Give the position of every leukocyte visible.
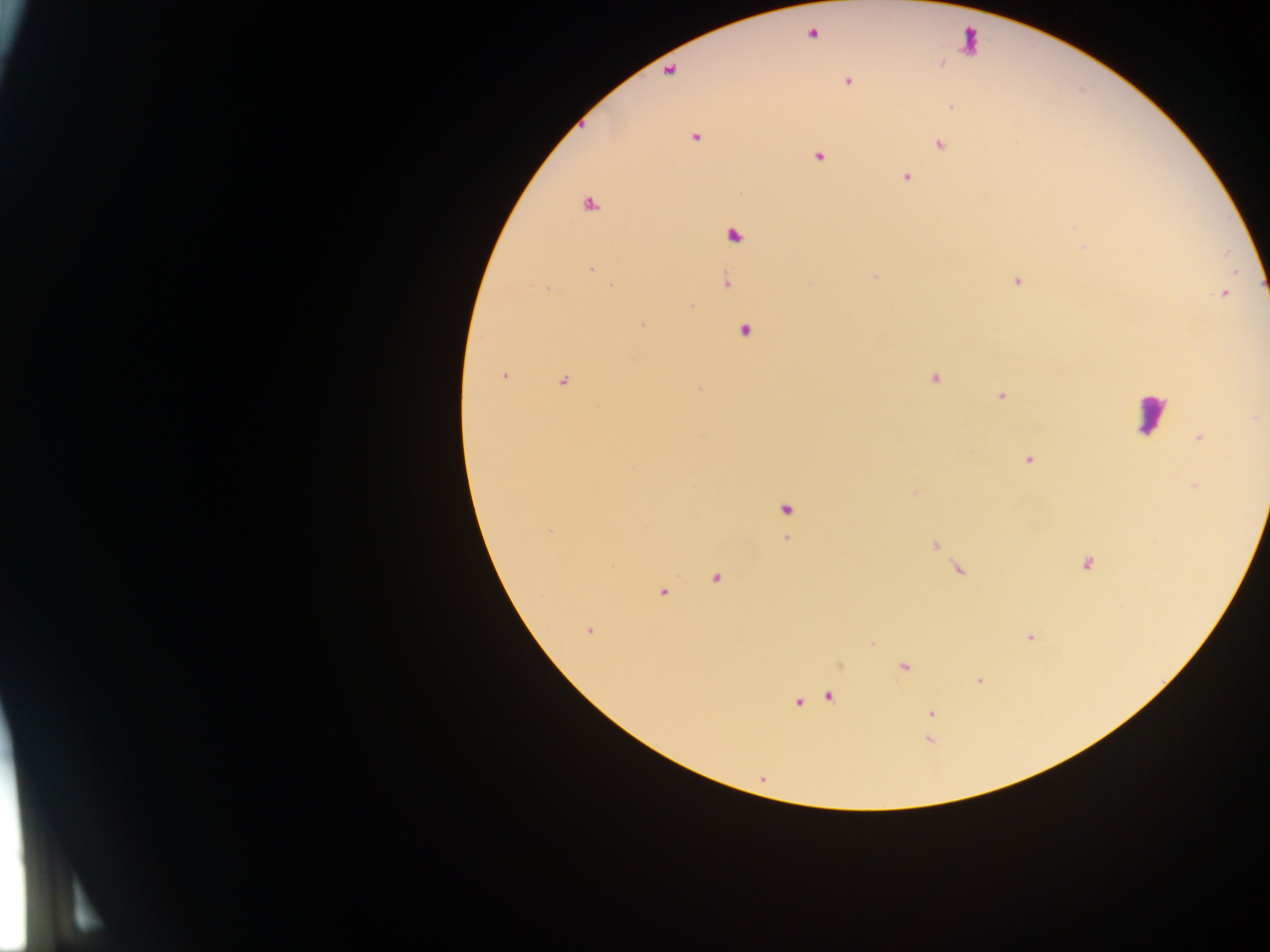
Approximate centers as [x, y] in pixels.
Leukocytes: [970, 42], [1150, 413].

Malaria parasite locations: [811, 34], [940, 63], [669, 70], [847, 81], [950, 106], [695, 136], [939, 145], [818, 156], [906, 176], [589, 203], [733, 234], [1084, 246], [591, 268], [875, 276], [725, 280], [1016, 280], [546, 289], [1223, 293], [690, 306], [643, 324], [744, 330], [503, 375], [933, 377], [562, 381], [700, 389], [1001, 396], [1256, 417], [1199, 437], [1027, 460], [1194, 486], [914, 493], [787, 509], [549, 531], [787, 539], [934, 544], [1087, 563], [958, 569], [716, 577], [662, 591], [589, 630], [1029, 637], [872, 643], [839, 664], [903, 666], [979, 680], [830, 695], [797, 702], [931, 713], [929, 740], [762, 779]. Image is 1270×952 pixels. Collected in Ghana. Single field of view. Thick blood film. Photographed through a microscope with a mobile-phone camera.